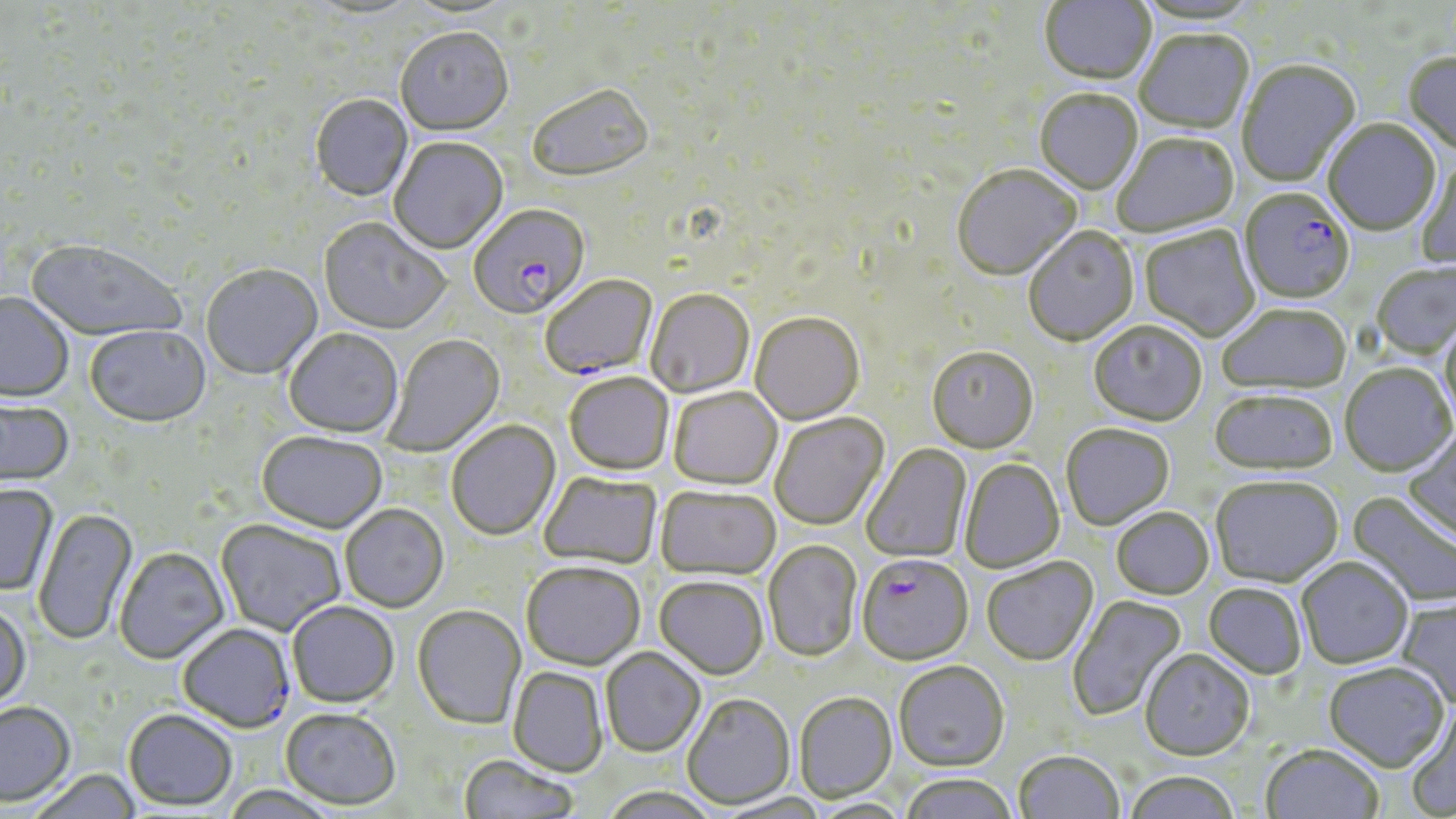
Approximate bounding boxes as (x1,y1)-(x2,y2) corner pairs in pixels. Uninfected red blood cell locations: (1039,0)-(1157,88), (1134,0)-(1262,27), (309,1)-(420,22), (401,1)-(519,21), (395,30)-(514,138), (1135,31)-(1254,135), (1403,53)-(1456,158), (1236,60)-(1361,188), (528,86)-(655,186), (1034,91)-(1143,196), (310,95)-(413,203), (1323,121)-(1441,237), (1113,134)-(1240,238), (389,139)-(508,255), (1413,156)-(1456,271), (951,166)-(1082,284), (318,219)-(451,337), (1140,226)-(1260,342), (1023,228)-(1139,347), (27,241)-(188,344), (1371,262)-(1456,360), (201,265)-(323,382), (645,290)-(755,399), (0,293)-(73,403), (1218,304)-(1352,395), (750,313)-(865,426), (1439,318)-(1456,432), (1088,321)-(1207,427), (84,327)-(212,429), (283,330)-(404,439), (384,334)-(505,457), (927,347)-(1039,455), (1339,364)-(1455,477), (564,373)-(674,476), (668,388)-(782,489), (1209,390)-(1338,475), (0,396)-(75,489), (770,413)-(890,531), (446,421)-(561,541), (1060,423)-(1174,530), (1402,427)-(1456,546), (256,432)-(387,535), (861,444)-(972,565), (959,458)-(1064,572), (538,471)-(662,570), (1210,476)-(1343,587), (0,485)-(58,596), (656,486)-(781,580), (1348,491)-(1456,610), (340,504)-(448,613), (1111,507)-(1215,599), (33,508)-(139,646), (215,520)-(346,637), (763,540)-(862,662), (115,548)-(230,665), (982,557)-(1098,667), (1296,557)-(1413,669), (521,562)-(645,671), (654,577)-(769,680), (1203,583)-(1307,679), (1067,594)-(1188,722), (1395,597)-(1456,709), (0,602)-(31,714), (287,602)-(400,709), (412,606)-(526,730), (600,648)-(706,757), (1139,648)-(1255,761), (893,661)-(1009,772), (1323,661)-(1449,771), (508,668)-(609,778), (794,692)-(898,803), (681,693)-(796,810), (0,703)-(76,808), (1403,703)-(1456,818), (280,709)-(401,811), (123,710)-(237,812), (1260,744)-(1384,819), (1013,751)-(1124,819), (459,755)-(580,819), (29,770)-(142,819), (1123,771)-(1242,819), (899,773)-(1019,819), (599,786)-(720,819), (218,787)-(343,819), (714,793)-(833,818). Plasmodium falciparum-infected red blood cell locations: (1239,190)-(1355,305), (469,207)-(590,322), (541,276)-(658,380), (857,554)-(973,666), (178,625)-(295,734). Slide-level diagnosis: Plasmodium falciparum. Single field of view. 1000x magnification. Thin blood smear. Light microscopy. Image is 1456×819 pixels. May-Grünwald-Giemsa stain.